Assess the morphology of the red blood cells.
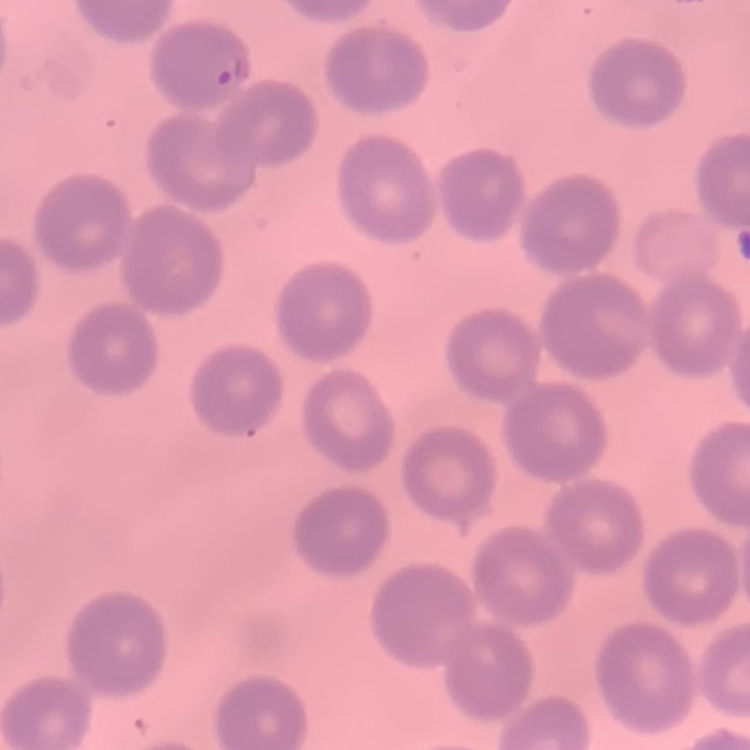

No rouleaux formation.

Stained with either Field's or Giemsa. Thin blood film. Square crop of a larger photomicrograph.